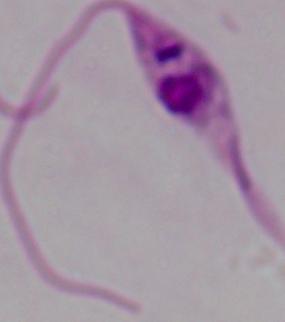 Captured at 1000x magnification. Photomicrograph. A Leishmania parasite is shown.